State which cell type is depicted.
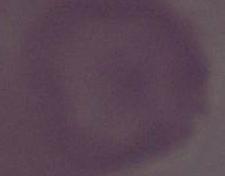
An erythrocyte.

Summary:
  - Modality: photomicrograph
  - Magnification: 1000x